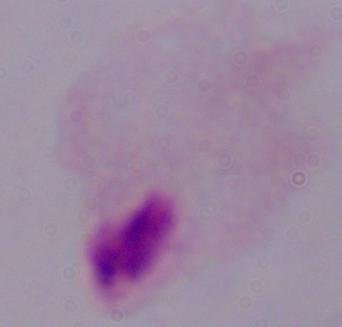
Photomicrograph. 1000x magnification. A trichomonad is seen.